Describe the morphology of the erythrocytes.
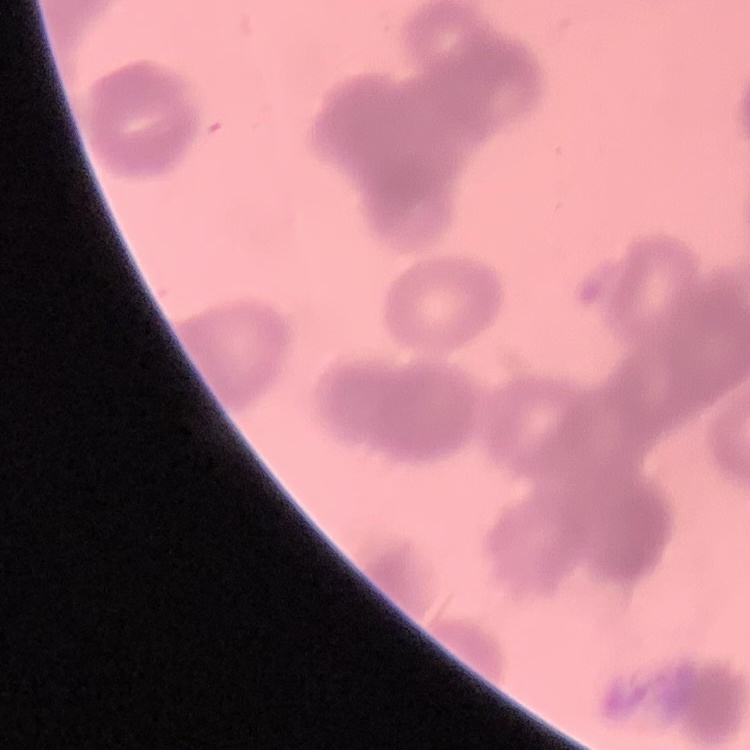

They show rouleaux formation.

Summary:
  - Preparation: thin blood film
  - Image type: square crop of a larger photomicrograph
  - Stain: Field's or Giemsa